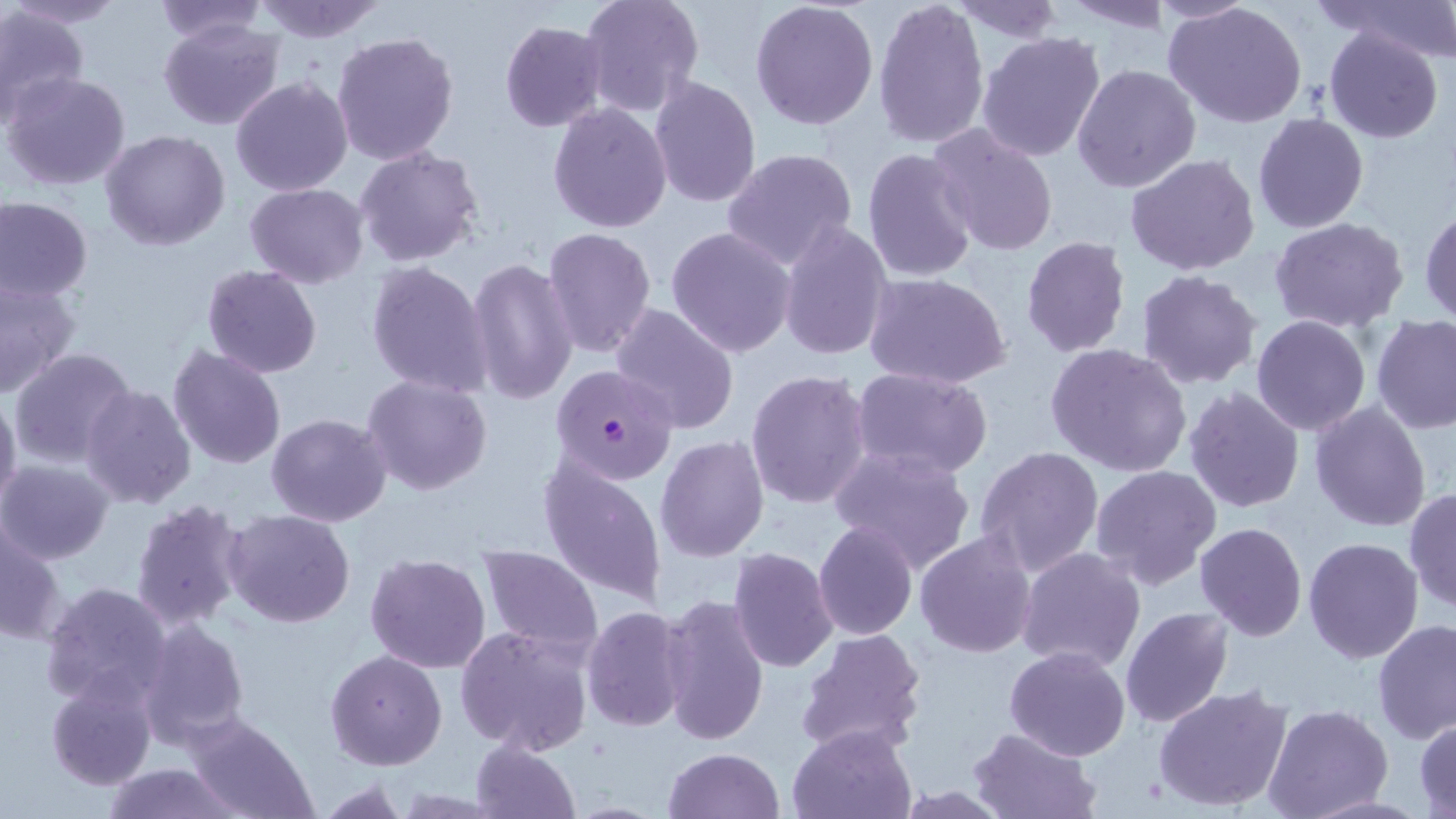
Approximate bounding boxes as named x1/y1/x2/y2 corners in pixels. Uninfected red blood cell locations: (x1=152, y1=0, x2=271, y2=46), (x1=579, y1=0, x2=706, y2=117), (x1=873, y1=0, x2=991, y2=151), (x1=1330, y1=0, x2=1455, y2=65), (x1=251, y1=1, x2=389, y2=43), (x1=750, y1=1, x2=880, y2=133), (x1=1059, y1=1, x2=1173, y2=32), (x1=1151, y1=1, x2=1262, y2=25), (x1=6, y1=2, x2=128, y2=28), (x1=948, y1=3, x2=1066, y2=44), (x1=1163, y1=3, x2=1308, y2=129), (x1=0, y1=4, x2=89, y2=122), (x1=159, y1=18, x2=284, y2=131), (x1=499, y1=20, x2=607, y2=131), (x1=1324, y1=27, x2=1443, y2=143), (x1=976, y1=30, x2=1108, y2=165), (x1=331, y1=31, x2=458, y2=167), (x1=1071, y1=63, x2=1201, y2=192), (x1=3, y1=71, x2=132, y2=191), (x1=230, y1=75, x2=353, y2=196), (x1=648, y1=76, x2=761, y2=210), (x1=548, y1=103, x2=672, y2=232), (x1=1251, y1=113, x2=1369, y2=234), (x1=925, y1=123, x2=1060, y2=259), (x1=99, y1=130, x2=230, y2=251), (x1=354, y1=146, x2=484, y2=267), (x1=722, y1=148, x2=859, y2=274), (x1=862, y1=148, x2=979, y2=282), (x1=1125, y1=154, x2=1261, y2=276), (x1=245, y1=182, x2=369, y2=287), (x1=1, y1=196, x2=92, y2=301), (x1=1419, y1=205, x2=1456, y2=327), (x1=1270, y1=216, x2=1409, y2=334), (x1=777, y1=219, x2=893, y2=364), (x1=665, y1=226, x2=798, y2=358), (x1=542, y1=227, x2=657, y2=360), (x1=1020, y1=237, x2=1131, y2=358), (x1=467, y1=256, x2=578, y2=406), (x1=367, y1=260, x2=492, y2=398), (x1=202, y1=265, x2=323, y2=379), (x1=1134, y1=270, x2=1262, y2=391), (x1=863, y1=273, x2=1011, y2=389), (x1=0, y1=277, x2=80, y2=397), (x1=610, y1=302, x2=740, y2=435), (x1=1251, y1=316, x2=1372, y2=436), (x1=1373, y1=317, x2=1456, y2=436), (x1=1044, y1=343, x2=1193, y2=480), (x1=168, y1=344, x2=287, y2=468), (x1=9, y1=346, x2=137, y2=469), (x1=852, y1=367, x2=992, y2=480), (x1=745, y1=369, x2=873, y2=509), (x1=362, y1=374, x2=493, y2=495), (x1=80, y1=384, x2=197, y2=510), (x1=1183, y1=386, x2=1306, y2=514), (x1=0, y1=388, x2=22, y2=514), (x1=1309, y1=400, x2=1433, y2=534), (x1=266, y1=413, x2=391, y2=527), (x1=654, y1=435, x2=769, y2=562), (x1=829, y1=444, x2=978, y2=574), (x1=974, y1=445, x2=1105, y2=579), (x1=538, y1=455, x2=667, y2=607), (x1=0, y1=460, x2=115, y2=564), (x1=1089, y1=464, x2=1220, y2=589), (x1=1404, y1=486, x2=1456, y2=612), (x1=130, y1=499, x2=252, y2=633), (x1=223, y1=509, x2=355, y2=628), (x1=2, y1=520, x2=66, y2=643), (x1=813, y1=521, x2=919, y2=640), (x1=1194, y1=522, x2=1307, y2=641), (x1=915, y1=532, x2=1037, y2=659), (x1=1302, y1=536, x2=1423, y2=664), (x1=475, y1=544, x2=605, y2=657), (x1=1017, y1=546, x2=1147, y2=674), (x1=727, y1=548, x2=839, y2=674), (x1=364, y1=553, x2=492, y2=674), (x1=39, y1=581, x2=172, y2=709), (x1=658, y1=594, x2=769, y2=745), (x1=582, y1=606, x2=690, y2=732), (x1=1118, y1=607, x2=1234, y2=729), (x1=135, y1=616, x2=250, y2=749), (x1=1372, y1=617, x2=1456, y2=743), (x1=456, y1=624, x2=592, y2=755), (x1=796, y1=626, x2=929, y2=756), (x1=1004, y1=645, x2=1132, y2=763), (x1=325, y1=648, x2=448, y2=771), (x1=46, y1=674, x2=157, y2=791), (x1=1154, y1=683, x2=1296, y2=813), (x1=1264, y1=705, x2=1393, y2=819), (x1=184, y1=715, x2=315, y2=819), (x1=1415, y1=717, x2=1456, y2=816), (x1=789, y1=725, x2=915, y2=818), (x1=969, y1=727, x2=1099, y2=818), (x1=470, y1=740, x2=580, y2=819), (x1=663, y1=748, x2=783, y2=819), (x1=100, y1=762, x2=241, y2=818). Plasmodium falciparum-infected red blood cell locations: (x1=549, y1=362, x2=681, y2=484). Slide-level diagnosis: Plasmodium falciparum. Thin blood film. Optical microscopy. Image is 1456×819 pixels. May-Grünwald-Giemsa stain. Single field of view. 1000x magnification.